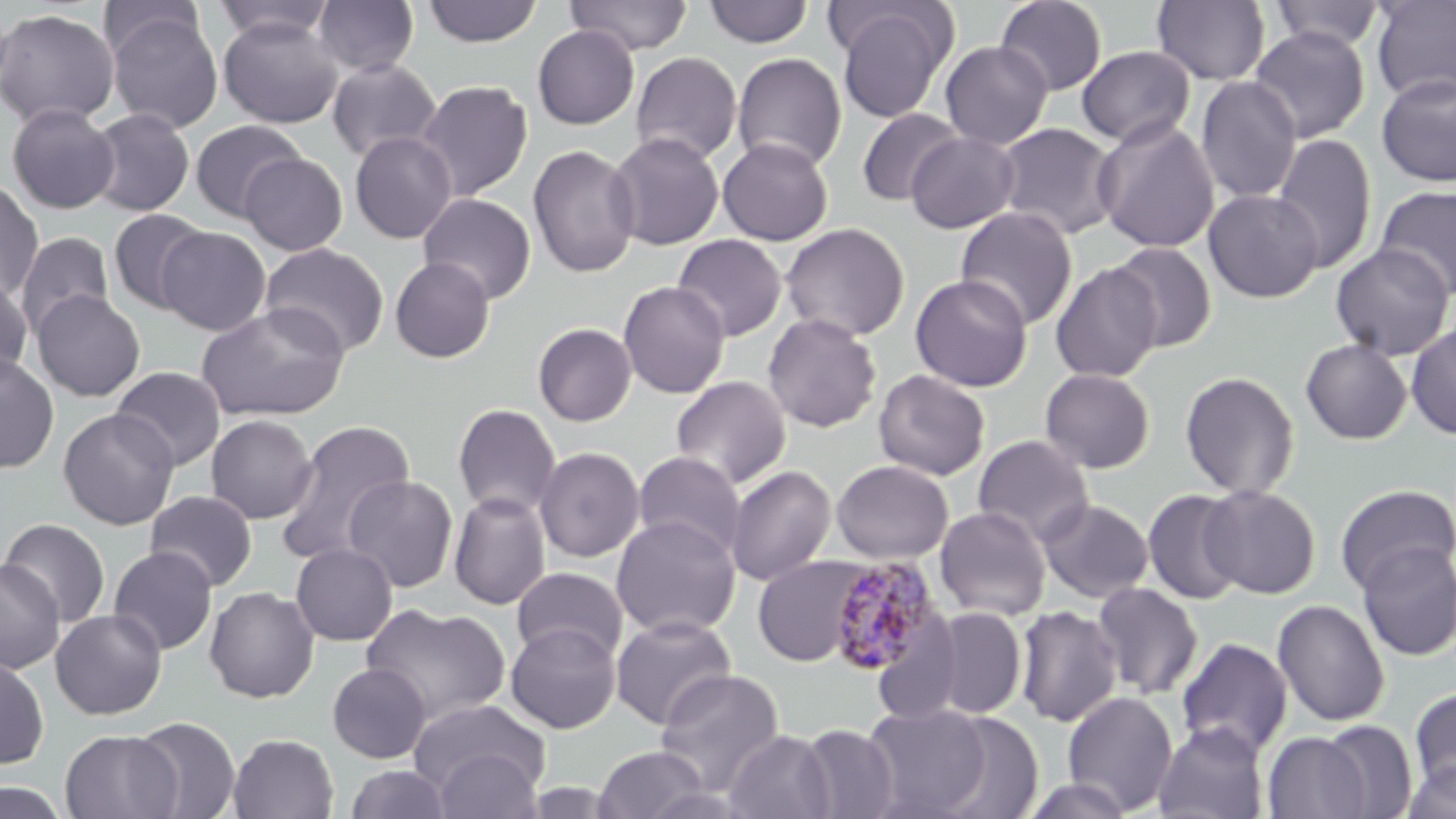
{
  "slide_level_diagnosis": "Plasmodium malariae",
  "stain": "May-Grünwald-Giemsa",
  "uninfected_red_blood_cell_locations": "approximate bounding boxes as named x1/y1/x2/y2 corners in pixels: (x1=98, y1=0, x2=205, y2=62), (x1=212, y1=0, x2=335, y2=43), (x1=312, y1=0, x2=419, y2=77), (x1=422, y1=0, x2=543, y2=48), (x1=565, y1=0, x2=693, y2=56), (x1=1369, y1=0, x2=1456, y2=104), (x1=704, y1=1, x2=813, y2=48), (x1=995, y1=1, x2=1107, y2=96), (x1=1151, y1=1, x2=1271, y2=86), (x1=1268, y1=1, x2=1387, y2=53), (x1=833, y1=5, x2=955, y2=123), (x1=0, y1=8, x2=119, y2=128), (x1=105, y1=9, x2=223, y2=133), (x1=218, y1=16, x2=342, y2=128), (x1=532, y1=25, x2=640, y2=129), (x1=1248, y1=25, x2=1371, y2=143), (x1=940, y1=40, x2=1053, y2=150), (x1=1076, y1=46, x2=1196, y2=149), (x1=630, y1=51, x2=743, y2=166), (x1=731, y1=53, x2=847, y2=173), (x1=326, y1=58, x2=442, y2=164), (x1=1376, y1=73, x2=1456, y2=187), (x1=1196, y1=76, x2=1302, y2=204), (x1=416, y1=80, x2=532, y2=202), (x1=7, y1=103, x2=120, y2=214), (x1=87, y1=108, x2=195, y2=217), (x1=855, y1=108, x2=965, y2=207), (x1=1094, y1=118, x2=1220, y2=254), (x1=189, y1=120, x2=304, y2=222), (x1=993, y1=122, x2=1120, y2=240), (x1=349, y1=130, x2=457, y2=244), (x1=905, y1=130, x2=1020, y2=234), (x1=607, y1=131, x2=725, y2=250), (x1=1270, y1=133, x2=1377, y2=273), (x1=717, y1=137, x2=833, y2=246), (x1=527, y1=143, x2=640, y2=279), (x1=240, y1=153, x2=347, y2=256), (x1=0, y1=179, x2=44, y2=301), (x1=1374, y1=185, x2=1456, y2=300), (x1=1204, y1=188, x2=1324, y2=303), (x1=417, y1=192, x2=537, y2=305), (x1=955, y1=206, x2=1078, y2=330), (x1=108, y1=209, x2=211, y2=314), (x1=780, y1=223, x2=910, y2=342), (x1=156, y1=227, x2=271, y2=335), (x1=15, y1=232, x2=114, y2=338), (x1=672, y1=233, x2=787, y2=341), (x1=1330, y1=242, x2=1454, y2=361), (x1=261, y1=243, x2=389, y2=358), (x1=1108, y1=243, x2=1218, y2=352), (x1=390, y1=257, x2=495, y2=363), (x1=1050, y1=262, x2=1163, y2=383), (x1=0, y1=272, x2=33, y2=380), (x1=910, y1=274, x2=1033, y2=392), (x1=617, y1=280, x2=730, y2=399), (x1=31, y1=290, x2=145, y2=402), (x1=196, y1=302, x2=349, y2=422), (x1=762, y1=313, x2=882, y2=433), (x1=1406, y1=321, x2=1456, y2=440), (x1=532, y1=322, x2=637, y2=427), (x1=1300, y1=339, x2=1412, y2=444), (x1=0, y1=352, x2=58, y2=474), (x1=110, y1=366, x2=226, y2=472), (x1=873, y1=368, x2=991, y2=481), (x1=1039, y1=368, x2=1156, y2=474), (x1=1179, y1=370, x2=1301, y2=501), (x1=670, y1=375, x2=791, y2=490), (x1=452, y1=403, x2=562, y2=519), (x1=57, y1=408, x2=180, y2=530), (x1=206, y1=414, x2=317, y2=524), (x1=274, y1=419, x2=418, y2=565), (x1=972, y1=434, x2=1094, y2=546), (x1=534, y1=445, x2=644, y2=563), (x1=632, y1=451, x2=746, y2=560), (x1=831, y1=459, x2=953, y2=564), (x1=726, y1=464, x2=836, y2=586), (x1=343, y1=474, x2=459, y2=593), (x1=1200, y1=484, x2=1320, y2=598), (x1=1334, y1=484, x2=1455, y2=595), (x1=1142, y1=488, x2=1248, y2=605), (x1=144, y1=490, x2=258, y2=592), (x1=448, y1=491, x2=551, y2=610), (x1=1037, y1=498, x2=1154, y2=603), (x1=935, y1=506, x2=1051, y2=621), (x1=611, y1=515, x2=741, y2=638), (x1=0, y1=517, x2=111, y2=627), (x1=1356, y1=540, x2=1456, y2=661), (x1=290, y1=543, x2=398, y2=646), (x1=108, y1=546, x2=218, y2=655), (x1=752, y1=555, x2=869, y2=667), (x1=0, y1=558, x2=66, y2=674), (x1=511, y1=567, x2=628, y2=667), (x1=1092, y1=582, x2=1203, y2=700), (x1=204, y1=586, x2=320, y2=703), (x1=1272, y1=599, x2=1390, y2=727), (x1=361, y1=603, x2=511, y2=727), (x1=1014, y1=605, x2=1122, y2=727), (x1=925, y1=607, x2=1027, y2=720), (x1=50, y1=610, x2=168, y2=719), (x1=611, y1=614, x2=737, y2=730), (x1=505, y1=622, x2=621, y2=733), (x1=1176, y1=637, x2=1293, y2=759), (x1=0, y1=655, x2=50, y2=769), (x1=327, y1=663, x2=431, y2=763), (x1=654, y1=669, x2=785, y2=797), (x1=1409, y1=687, x2=1456, y2=796), (x1=1062, y1=691, x2=1179, y2=814), (x1=407, y1=698, x2=550, y2=804), (x1=862, y1=704, x2=992, y2=817), (x1=932, y1=711, x2=1044, y2=819), (x1=129, y1=716, x2=241, y2=819), (x1=1316, y1=719, x2=1417, y2=818), (x1=1153, y1=722, x2=1270, y2=819), (x1=797, y1=723, x2=899, y2=818), (x1=60, y1=729, x2=181, y2=818), (x1=724, y1=730, x2=836, y2=819), (x1=1263, y1=731, x2=1370, y2=819), (x1=228, y1=733, x2=339, y2=819), (x1=593, y1=745, x2=709, y2=819), (x1=430, y1=747, x2=544, y2=819), (x1=1404, y1=758, x2=1456, y2=819), (x1=344, y1=764, x2=453, y2=818), (x1=1022, y1=776, x2=1135, y2=819), (x1=0, y1=780, x2=72, y2=819)",
  "image_size": "1456×819 pixels",
  "preparation": "thin blood smear",
  "magnification": "1000x",
  "plasmodium_malariae_infected_red_blood_cell_locations": "approximate bounding boxes as named x1/y1/x2/y2 corners in pixels: (x1=825, y1=555, x2=943, y2=676)",
  "modality": "optical microscopy",
  "field_of_view": "one of a larger specimen"
}